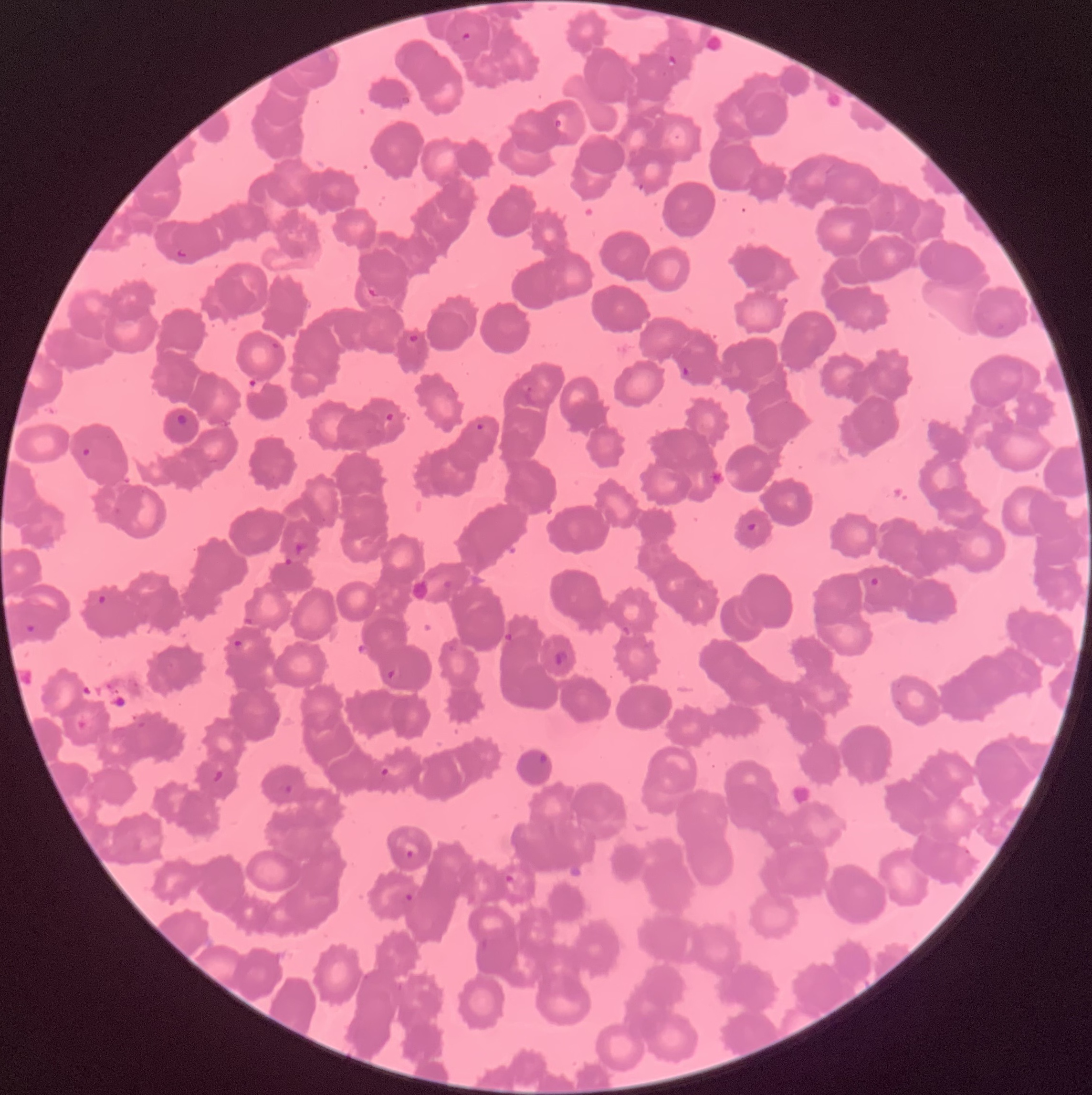

Approximate bounding boxes as [x1, y1, x2, y2] in pixels. Plasmodium parasite locations: [461, 31, 472, 42], [667, 54, 677, 68], [553, 117, 563, 131], [175, 248, 189, 260], [365, 284, 380, 299], [405, 333, 420, 347], [269, 340, 284, 353], [683, 366, 693, 377], [384, 411, 396, 422], [176, 413, 188, 427], [475, 423, 485, 432], [80, 446, 92, 459], [747, 522, 761, 534], [294, 541, 309, 555], [870, 576, 883, 588], [96, 594, 108, 605], [23, 623, 39, 636], [232, 638, 244, 649], [553, 649, 568, 666], [387, 669, 396, 680], [538, 752, 549, 765], [378, 767, 390, 777], [211, 769, 224, 783], [283, 785, 294, 795], [403, 848, 417, 861], [503, 873, 516, 886], [403, 891, 415, 904]. Light microscopy. Thin blood film. Image is 1092×1095 pixels. The red blood cells show rouleaux formation.